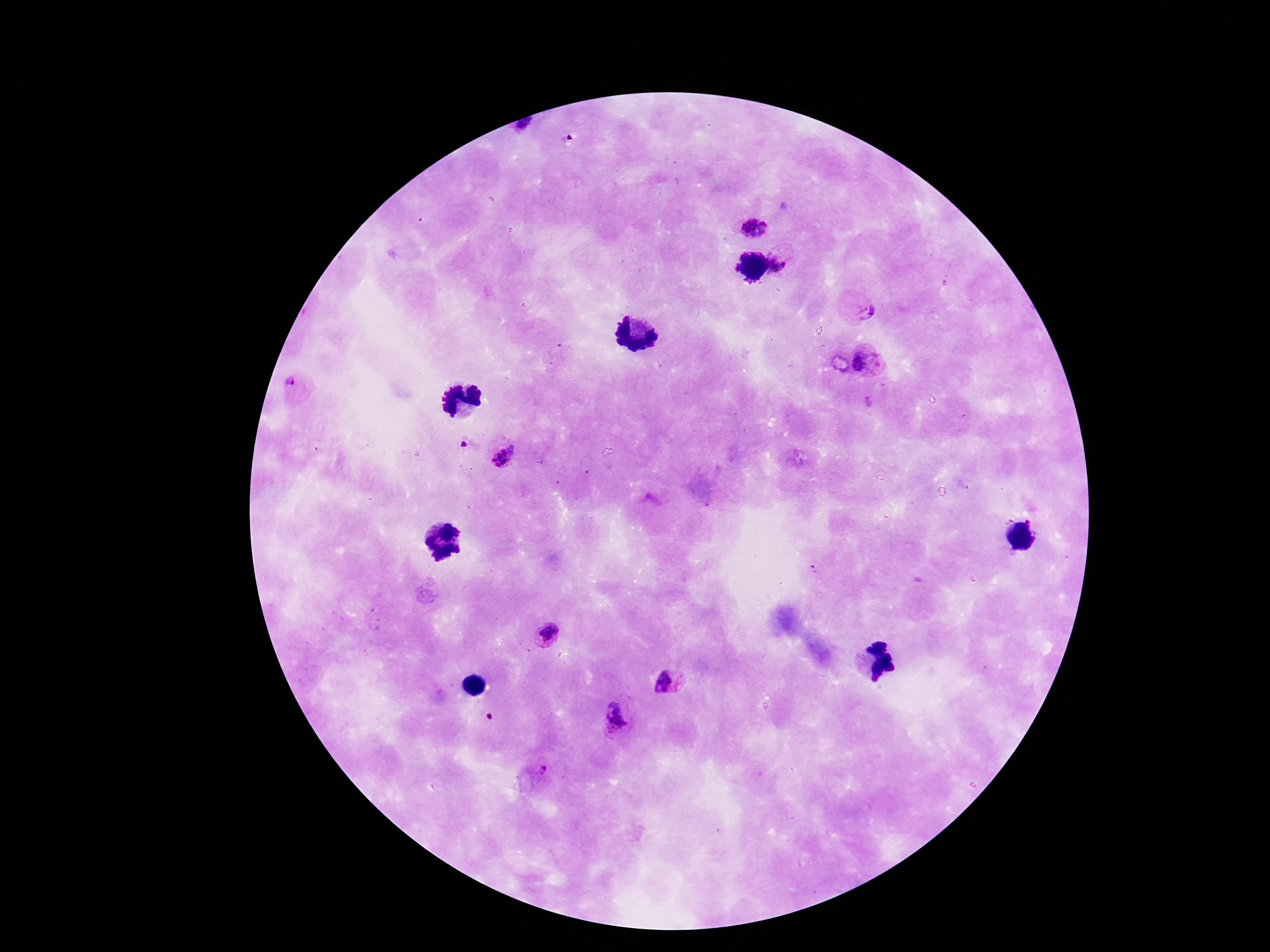
Approximate centers as {x, y} in pixels.
Summary:
  - Plasmodium parasite locations: {525, 127}, {753, 226}, {783, 259}, {863, 309}, {866, 361}, {295, 385}, {463, 445}, {502, 451}, {549, 634}, {669, 682}, {617, 717}, {539, 773}
  - Image size: 1270×952 pixels
  - Field of view: one from this slide
  - Stain: Giemsa
  - Magnification: 100x
  - Capture: smartphone camera through the microscope eyepiece
  - Patient malaria status: positive
  - Preparation: thick blood smear